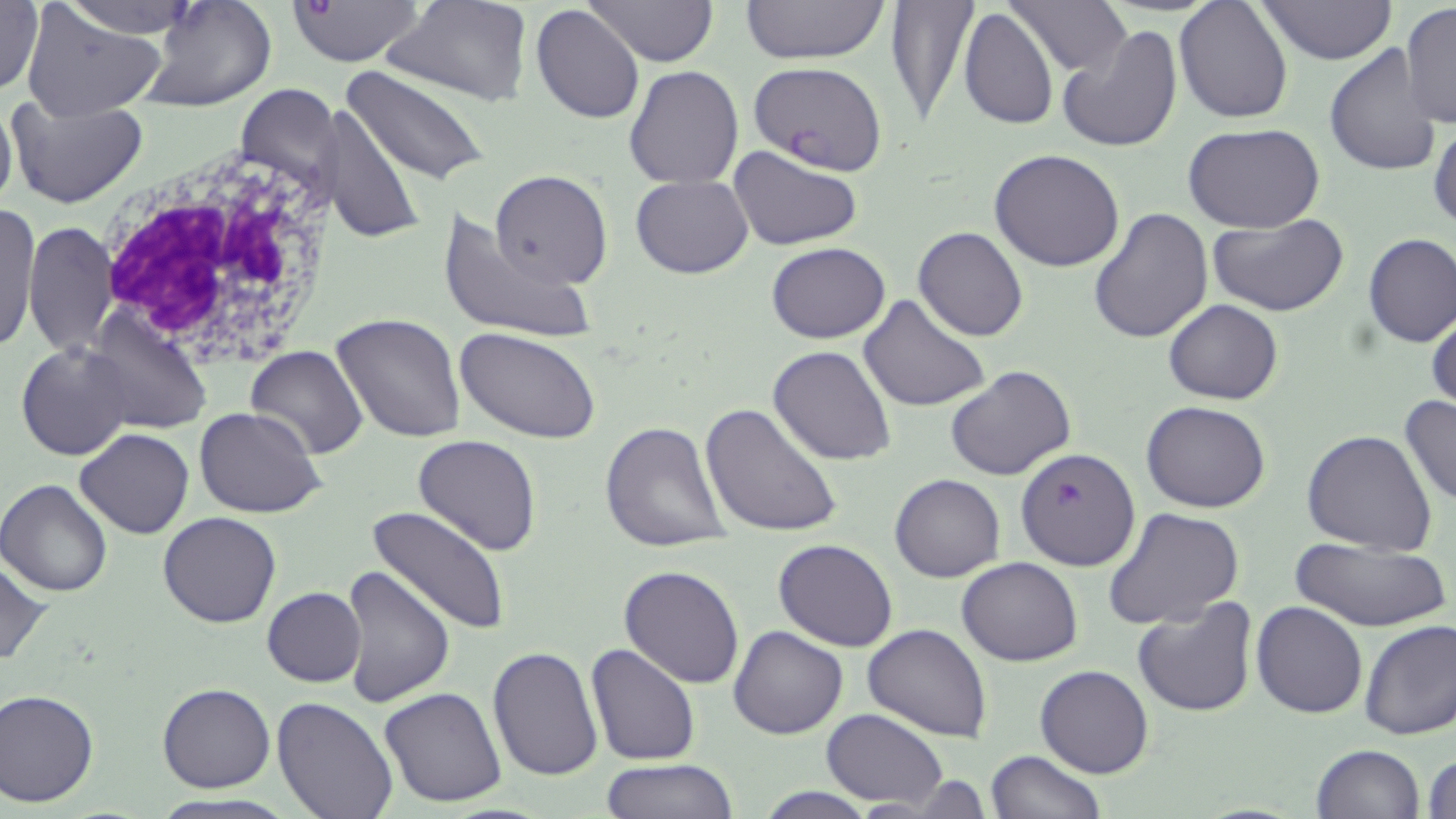

slide-level diagnosis = Plasmodium falciparum
stain = May-Grünwald-Giemsa
white blood cell locations = approximate bounding boxes as (x1,y1)-(x2,y2) corner pairs in pixels: (91,146)-(337,367)
field of view = one of a larger specimen
modality = optical microscopy
image size = 1456×819 pixels
preparation = thin blood smear
magnification = 1000x
Plasmodium falciparum-infected red blood cell locations = approximate bounding boxes as (x1,y1)-(x2,y2) corner pairs in pixels: (284,0)-(427,68), (751,60)-(889,174), (1014,446)-(1136,571)
uninfected red blood cell locations = approximate bounding boxes as (x1,y1)-(x2,y2) corner pairs in pixels: (58,0)-(203,39), (140,0)-(277,112), (584,0)-(717,66), (741,0)-(889,66), (882,0)-(978,123), (1008,0)-(1131,75), (1257,0)-(1397,64), (0,1)-(45,98), (385,1)-(530,106), (1174,1)-(1292,121), (1400,4)-(1456,130), (531,5)-(643,126), (17,8)-(163,120), (958,8)-(1057,131), (1056,23)-(1185,154), (1324,43)-(1443,177), (343,65)-(490,187), (625,66)-(744,189), (234,81)-(340,207), (0,91)-(17,223), (4,91)-(150,210), (324,103)-(425,246), (1429,118)-(1456,234), (1185,125)-(1324,235), (728,145)-(863,251), (988,148)-(1125,272), (490,170)-(614,288), (631,175)-(752,279), (3,206)-(40,354), (437,206)-(595,345), (1088,206)-(1215,344), (1209,214)-(1352,317), (24,221)-(119,358), (913,226)-(1028,342), (1362,233)-(1456,346), (766,242)-(891,343), (859,295)-(988,412), (1163,299)-(1283,404), (85,309)-(214,436), (1427,311)-(1456,416), (331,313)-(467,444), (457,329)-(601,443), (16,342)-(132,461), (245,345)-(367,459), (768,345)-(896,465), (945,364)-(1076,480), (1399,395)-(1456,508), (1141,400)-(1272,513), (699,401)-(844,540), (194,407)-(326,518), (600,423)-(730,553), (76,428)-(194,540), (1303,430)-(1438,554), (412,434)-(544,557), (890,474)-(1004,583), (0,478)-(114,598), (369,505)-(507,635), (1103,506)-(1244,630), (157,512)-(283,628), (1286,536)-(1453,634), (773,539)-(899,652), (0,556)-(50,669), (956,556)-(1082,666), (335,565)-(453,708), (620,565)-(744,688), (261,587)-(366,686), (1131,594)-(1258,717), (1251,602)-(1368,719), (1358,618)-(1456,741), (863,623)-(992,743), (729,625)-(847,740), (585,642)-(699,767), (487,644)-(602,780), (1035,665)-(1153,779), (157,683)-(275,793), (380,687)-(508,807), (0,688)-(99,805), (273,697)-(398,819), (821,709)-(948,809), (1310,744)-(1424,819), (985,750)-(1106,819), (1424,752)-(1456,819), (600,759)-(739,817), (749,787)-(885,818)